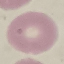

result = no malaria parasites seen
stain = Giemsa
capture = smartphone through the microscope eyepiece
image type = cell patch, automatically extracted from a larger field of view and resized to 64 × 64 pixels
preparation = thin blood smear